Report the malaria status of this cell.
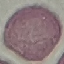
It is uninfected.

Thin smear of blood. Photographed with a smartphone camera at the microscope eyepiece. Automatically extracted cell patch, resized to 64 × 64 pixels. Giemsa stain.